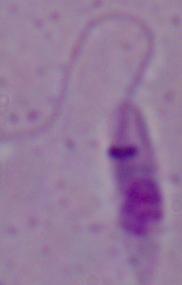
{
  "magnification": "1000x",
  "modality": "photomicrograph",
  "identification": "Leishmania"
}